Locate every Plasmodium parasite.
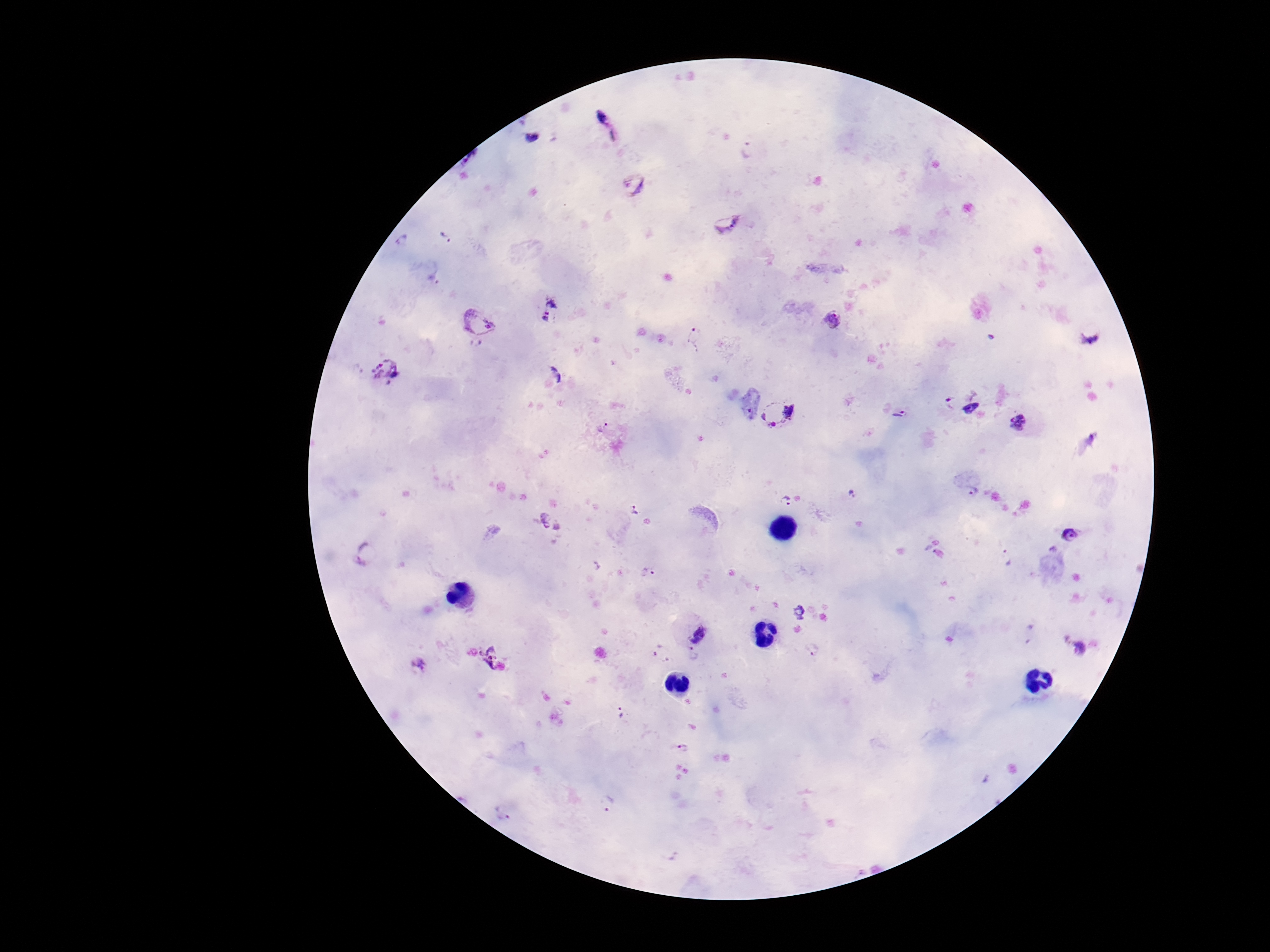

Approximate object centers, in pixels from the top-left corner.
Plasmodium parasites: (x=605, y=120), (x=533, y=137), (x=747, y=149), (x=634, y=186), (x=726, y=221), (x=445, y=236), (x=403, y=240), (x=550, y=309), (x=832, y=319), (x=478, y=326), (x=1090, y=334), (x=695, y=337), (x=387, y=370), (x=557, y=375), (x=950, y=402), (x=970, y=407), (x=900, y=413), (x=782, y=414), (x=1019, y=421), (x=604, y=427), (x=972, y=492), (x=853, y=495), (x=786, y=502), (x=634, y=509), (x=551, y=522), (x=1071, y=535), (x=366, y=552), (x=1007, y=556), (x=648, y=573), (x=1030, y=632), (x=695, y=633), (x=658, y=648), (x=1079, y=648), (x=814, y=650), (x=693, y=657), (x=493, y=658), (x=419, y=665), (x=620, y=713), (x=684, y=748), (x=609, y=803), (x=503, y=813).

patient_malaria_status: infected
capture: smartphone camera through the microscope eyepiece
stain: Giemsa
image_size: 1270×952 pixels
magnification: 100x
preparation: thick blood smear
field_of_view: one from this slide